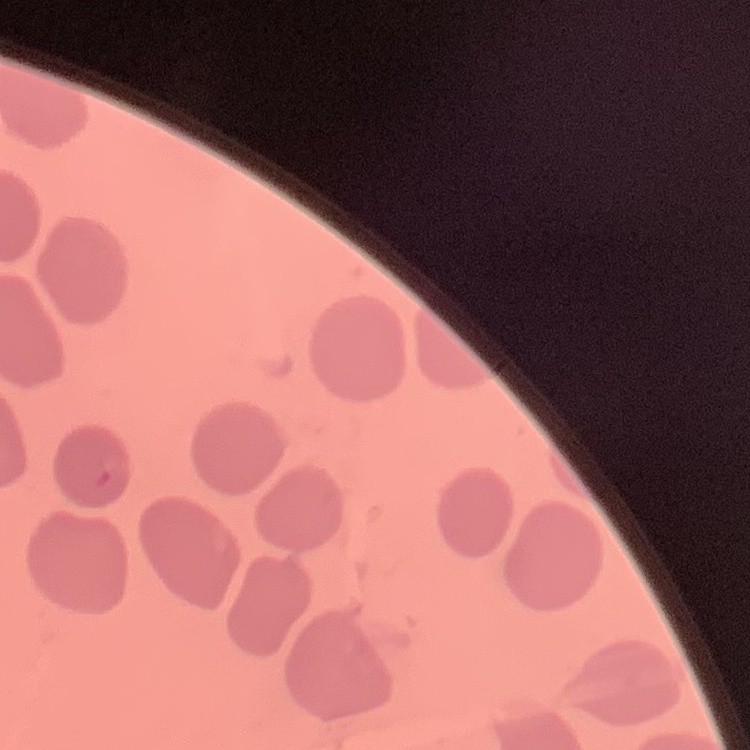
The erythrocytes exhibit no rouleaux formation. Square crop of a larger photomicrograph. Stained with either Field's or Giemsa. Thin peripheral smear.